Give the extent of all Plasmodium vivax-infected red blood cells.
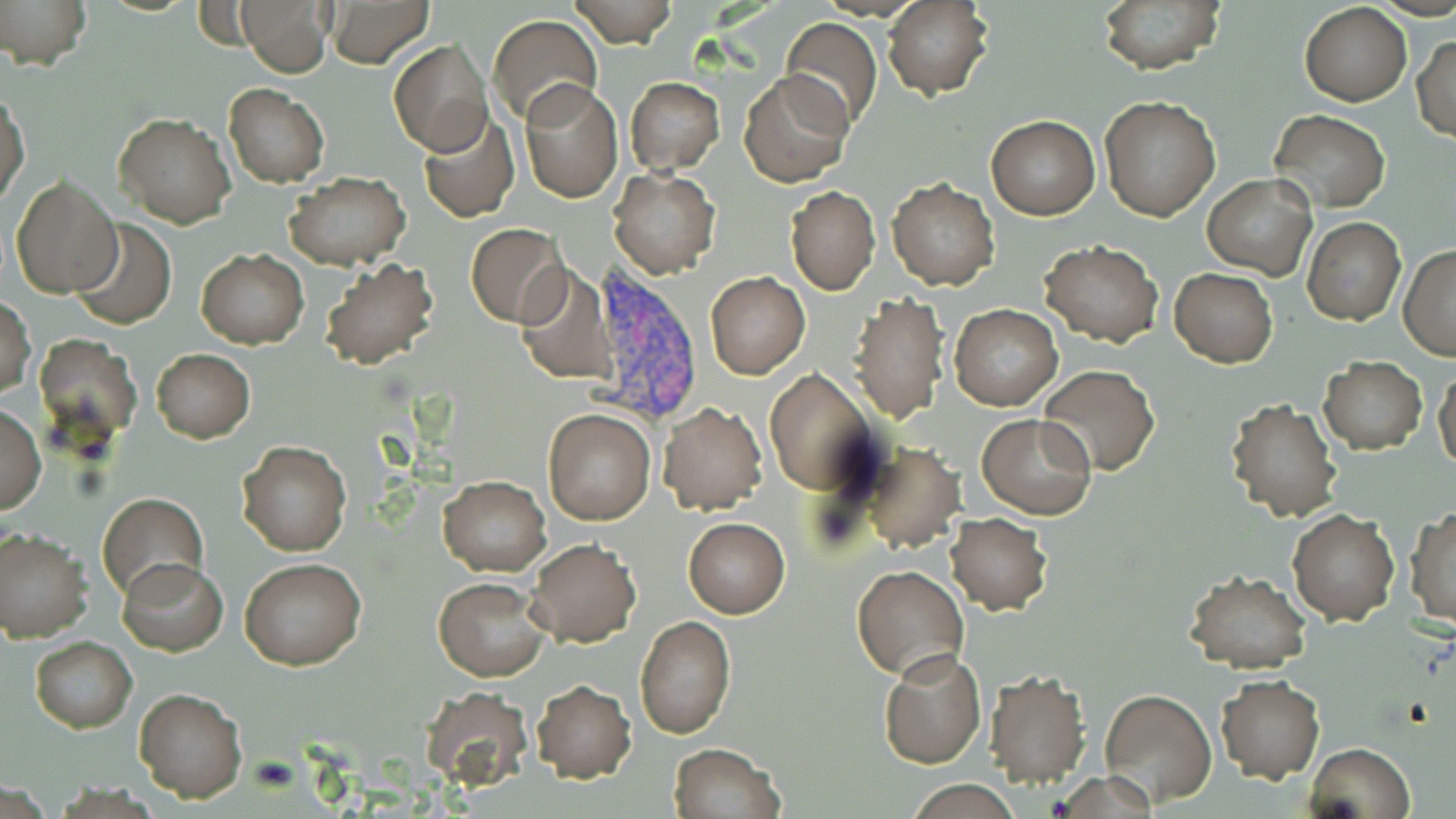
Approximate bounding boxes as [x1, y1, x2, y2] in pixels.
Plasmodium vivax-infected red blood cells: [584, 267, 704, 425].

Uninfected red blood cell locations: [0, 0, 90, 69], [236, 0, 332, 76], [324, 0, 434, 68], [564, 0, 680, 48], [884, 0, 994, 101], [1095, 0, 1225, 74], [1299, 1, 1413, 106], [487, 14, 603, 126], [779, 17, 883, 130], [1412, 34, 1455, 142], [388, 37, 492, 157], [738, 70, 853, 187], [625, 76, 725, 175], [518, 79, 622, 202], [224, 83, 329, 188], [1, 84, 29, 209], [1099, 97, 1222, 222], [1269, 109, 1389, 212], [113, 111, 236, 227], [416, 111, 520, 222], [986, 115, 1100, 219], [609, 168, 720, 277], [285, 171, 412, 271], [10, 173, 123, 299], [1203, 175, 1317, 279], [886, 177, 999, 290], [785, 186, 880, 295], [1301, 215, 1405, 326], [69, 218, 177, 329], [465, 222, 570, 328], [1040, 239, 1163, 347], [1399, 246, 1456, 360], [195, 248, 308, 348], [318, 255, 439, 371], [512, 266, 617, 385], [1170, 268, 1277, 368], [704, 272, 811, 379], [847, 292, 951, 427], [1, 298, 36, 399], [949, 304, 1061, 410], [33, 334, 142, 450], [151, 348, 255, 443], [1318, 357, 1427, 455], [1039, 363, 1160, 476], [1433, 367, 1456, 475], [766, 369, 879, 494], [1224, 396, 1342, 522], [659, 402, 768, 514], [0, 404, 45, 513], [543, 408, 655, 525], [978, 413, 1098, 520], [237, 439, 351, 556], [857, 442, 966, 554], [439, 475, 551, 576], [98, 493, 207, 604], [1407, 506, 1456, 629], [1287, 509, 1398, 625], [945, 512, 1053, 613], [682, 516, 790, 618], [0, 526, 92, 642], [525, 537, 641, 648], [117, 558, 229, 655], [240, 558, 366, 670], [850, 565, 970, 682], [1183, 569, 1312, 675], [432, 576, 549, 681], [635, 615, 736, 738], [29, 636, 138, 733], [878, 648, 986, 769], [880, 658, 1090, 779], [983, 669, 1092, 789], [1214, 676, 1324, 783], [531, 680, 637, 783], [132, 685, 248, 803], [419, 687, 535, 792], [1099, 687, 1217, 806], [1305, 742, 1415, 819], [668, 743, 784, 819], [902, 781, 1026, 816]. Slide-level diagnosis: Plasmodium vivax. Thin blood film. One field of a larger specimen. May-Grünwald-Giemsa stain. Image is 1456×819 pixels. Optical microscopy. 1000x magnification.